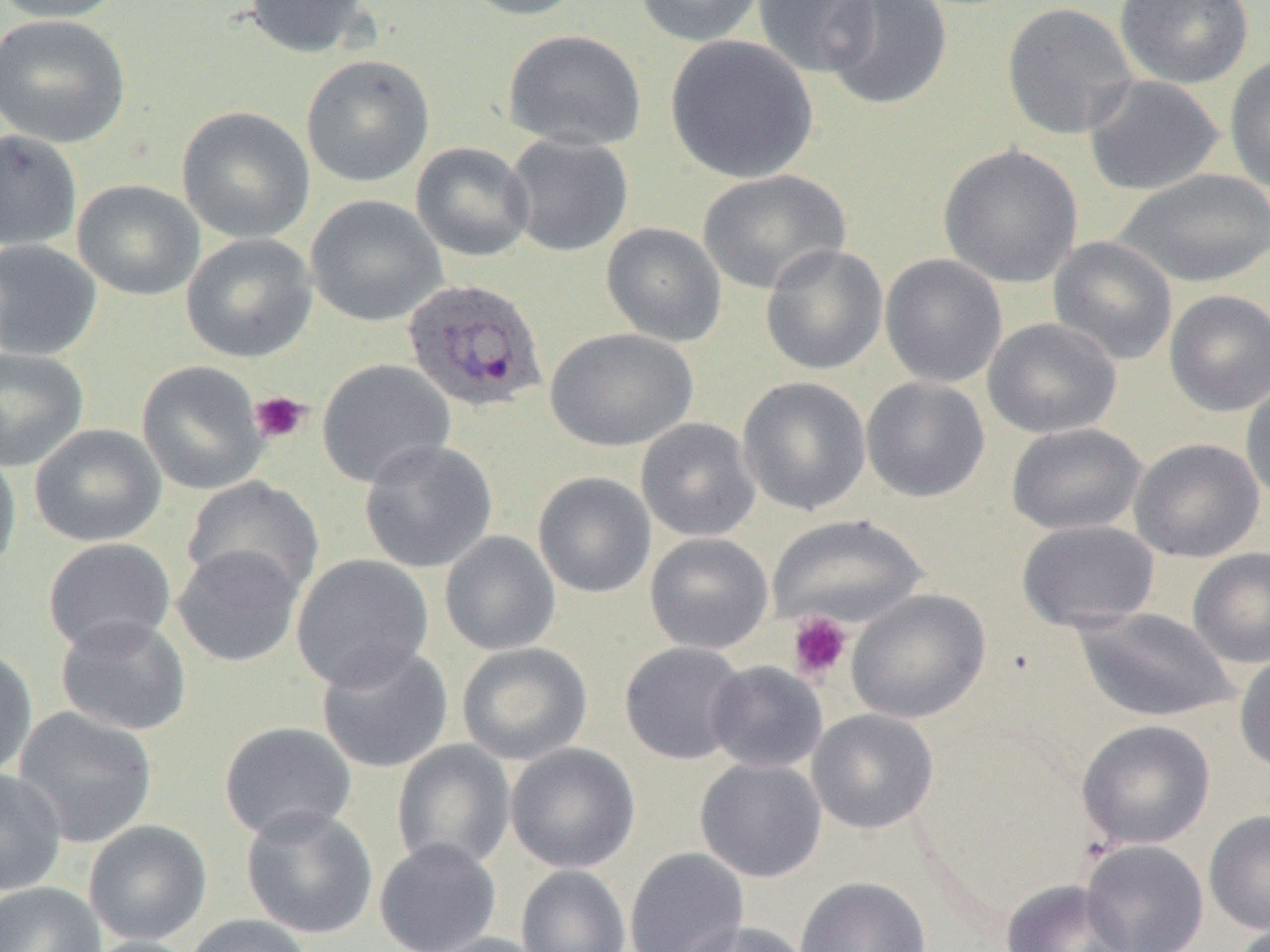
Summary:
  - Coordinate format: approximate bounding boxes as [x1, y1, x2, y2] in pixels
  - Uninfected red blood cell locations: [0, 0, 127, 23], [244, 0, 376, 58], [456, 0, 589, 21], [634, 0, 765, 47], [752, 0, 877, 78], [821, 0, 953, 111], [1114, 0, 1255, 89], [1001, 2, 1139, 140], [0, 13, 132, 148], [502, 29, 648, 152], [665, 34, 818, 183], [301, 54, 435, 187], [1224, 54, 1270, 194], [1083, 75, 1224, 196], [176, 106, 316, 244], [0, 128, 82, 251], [504, 132, 634, 257], [411, 142, 535, 262], [938, 144, 1083, 288], [1113, 167, 1270, 289], [698, 169, 851, 295], [72, 179, 206, 301], [305, 195, 447, 327], [601, 222, 728, 346], [181, 233, 317, 364], [1048, 236, 1178, 365], [0, 239, 102, 361], [760, 243, 888, 375], [880, 253, 1008, 388], [1164, 289, 1270, 416], [983, 317, 1122, 439], [545, 327, 697, 452], [0, 347, 89, 472], [317, 358, 455, 489], [136, 360, 269, 496], [737, 376, 872, 516], [861, 377, 990, 502], [1240, 379, 1270, 506], [635, 418, 761, 542], [1006, 422, 1147, 535], [29, 424, 167, 548], [1129, 437, 1265, 562], [359, 439, 498, 573], [0, 446, 22, 577], [532, 471, 656, 599], [182, 476, 325, 603], [768, 514, 929, 629], [1016, 520, 1160, 633], [439, 530, 561, 656], [645, 532, 774, 654], [42, 537, 177, 655], [171, 544, 304, 668], [1187, 547, 1270, 668], [290, 554, 434, 691], [846, 589, 990, 724], [1075, 607, 1236, 723], [54, 614, 192, 736], [315, 641, 454, 775], [620, 641, 751, 765], [456, 642, 593, 765], [0, 645, 38, 780], [1234, 653, 1270, 775], [706, 660, 828, 774], [13, 707, 158, 848], [807, 709, 939, 834], [1076, 719, 1216, 850], [218, 721, 357, 843], [391, 740, 516, 872], [505, 743, 640, 873], [695, 758, 827, 883], [0, 767, 67, 896], [240, 806, 379, 940], [1204, 809, 1270, 934], [82, 820, 213, 946], [373, 838, 502, 952], [1081, 838, 1209, 952], [624, 847, 749, 952], [516, 865, 631, 952], [795, 876, 932, 952], [1000, 878, 1135, 952], [0, 882, 107, 952], [183, 914, 315, 952], [680, 920, 812, 952], [418, 932, 553, 952], [79, 936, 203, 952]
  - Platelet locations: [249, 391, 312, 444], [787, 612, 852, 682]
  - Plasmodium ovale-infected red blood cell locations: [402, 277, 548, 413]
  - Slide-level diagnosis: Plasmodium ovale
  - Image size: 1270×952 pixels
  - Magnification: 1000x
  - Preparation: thin blood smear
  - Modality: light microscopy
  - Field of view: single